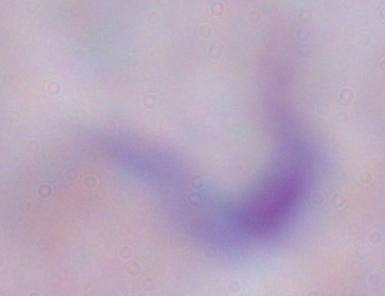
magnification = 1000x
identification = trypanosome
modality = micrograph